Report the malaria status of this cell.
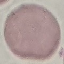
It is uninfected.

Giemsa stain. Photographed with a smartphone camera at the microscope eyepiece. Thin blood film. Automatically extracted cell patch, resized to 64 × 64 pixels.